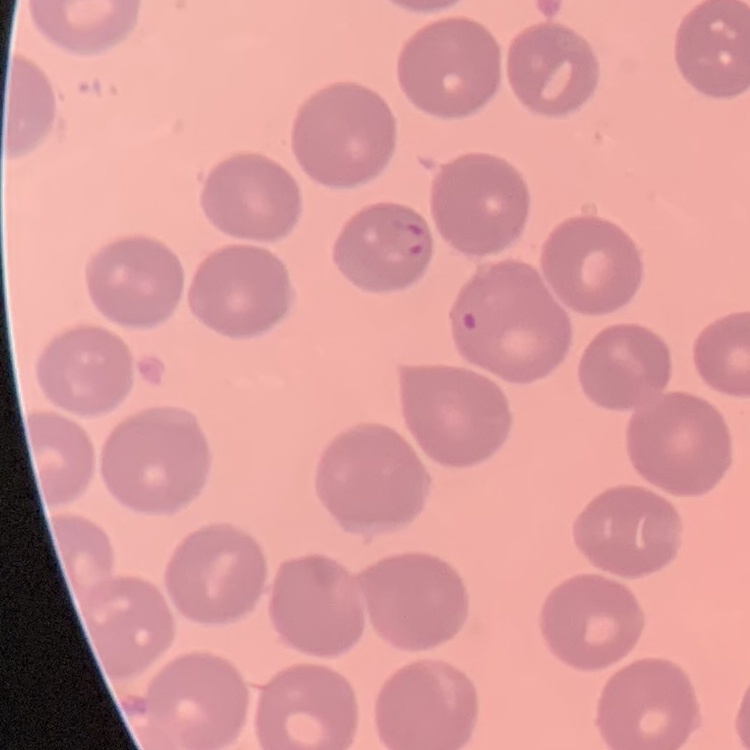
red_blood_cell_morphology: no rouleaux formation
stain: Field's or Giemsa
image_type: square crop of a larger photomicrograph
preparation: thin blood smear